Assess this cell for malaria.
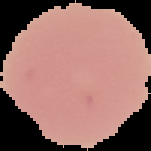

It is uninfected.

Image is 151×151 pixels. Cell region segmented out of the field of view; the surrounding area is masked to black. From a thin blood film.